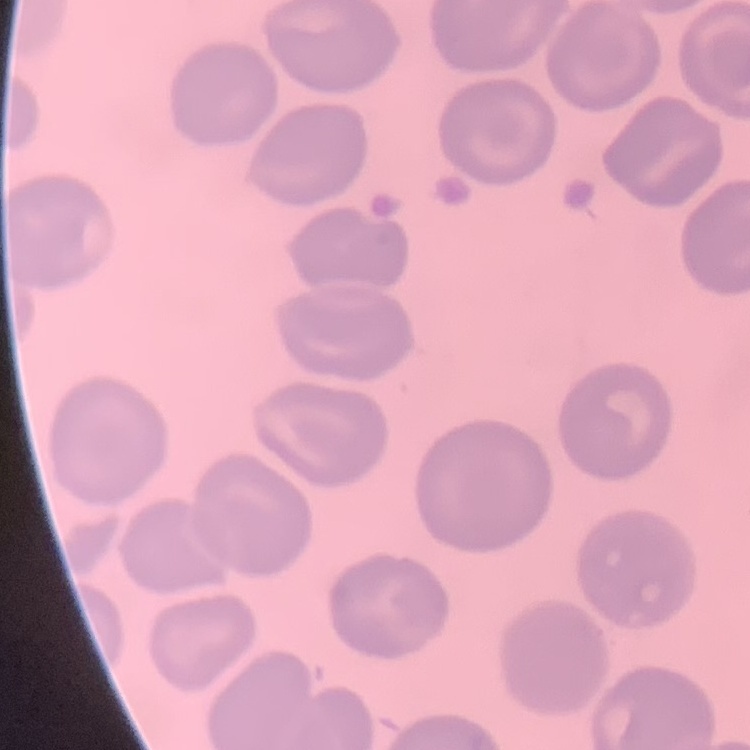

The erythrocytes exhibit no rouleaux formation. Thin peripheral smear. One tile cut from a larger photomicrograph. Field's or Giemsa stain.